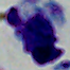

Summary:
  - Magnification: 1000x
  - Modality: micrograph
  - Identification: leukocyte